State which parasite is depicted.
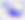
Toxoplasma gondii.

Captured at 400x magnification. Micrograph.